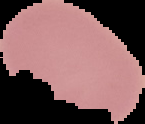
{
  "image_size": "145×124 pixels",
  "image_type": "segmented cell region on a black background",
  "result": "no malaria parasites detected",
  "preparation": "thin blood film"
}